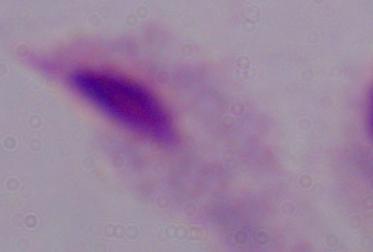
identification = trichomonad
modality = photomicrograph
magnification = 1000x